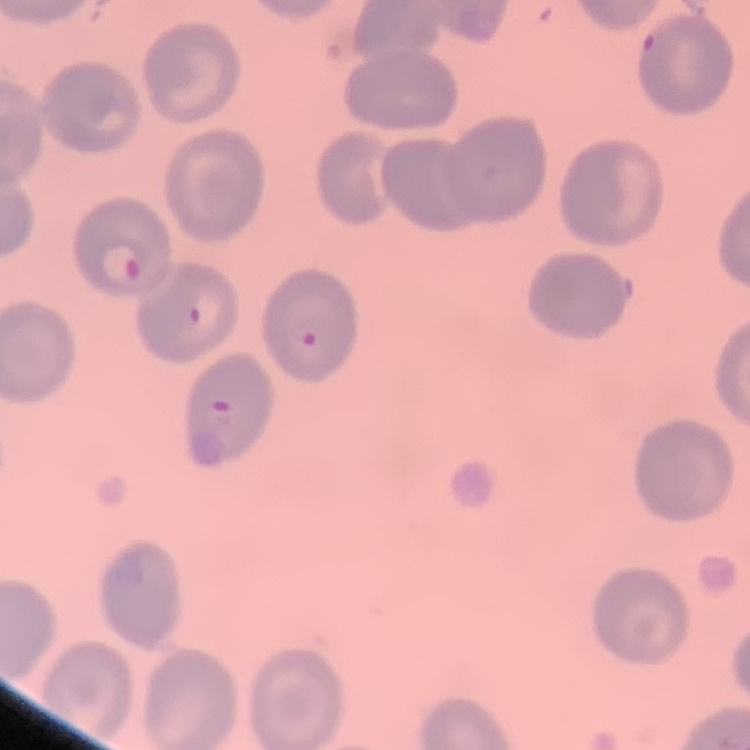

erythrocyte morphology = no rouleaux formation
stain = Field's or Giemsa
preparation = thin blood film
image type = square crop of a larger photomicrograph